Report the malaria status.
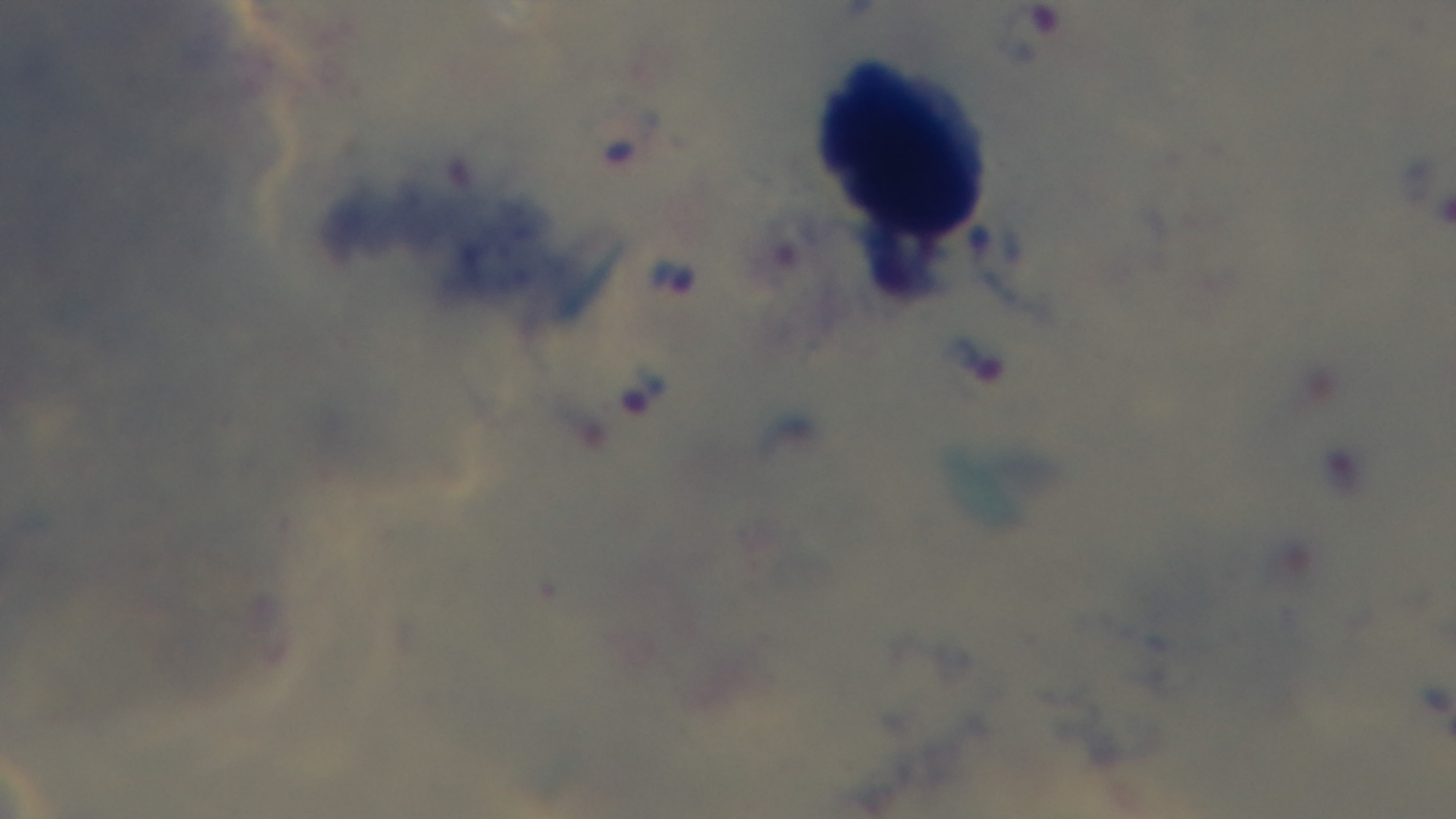

It is infected.

One field from the slide. Photomicrograph. Oil-immersion objective, 100x. Preparation: thick blood film. Giemsa-stained. Mounted 4K digital camera.